Name the parasite shown.
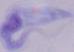
This is a trypanosome.

modality = micrograph
magnification = 1000x